State the preparation type.
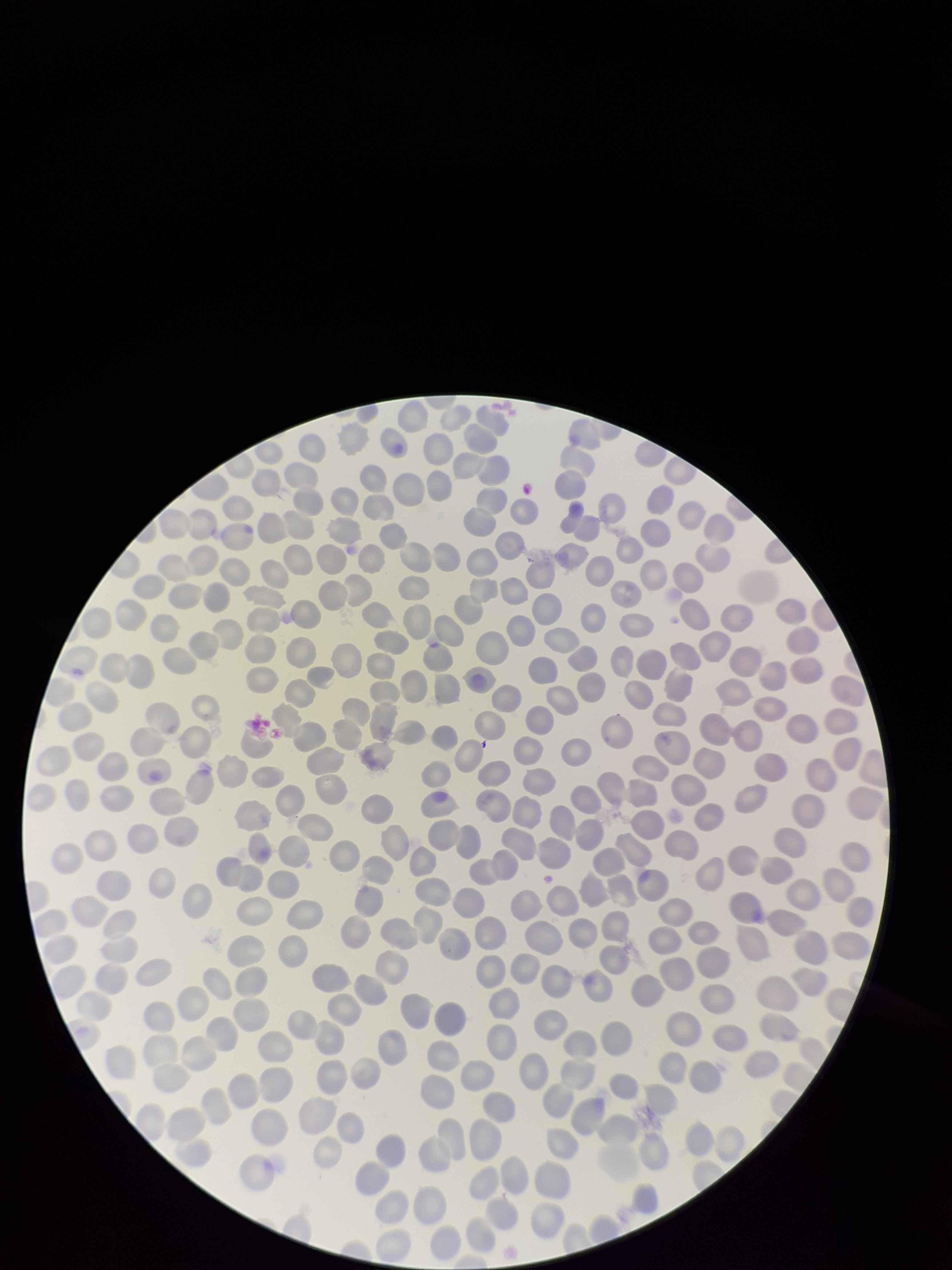
Thin.

Summary:
  - Patient malaria status: negative
  - Capture: smartphone photograph through the microscope eyepiece
  - Field of view: one from this slide
  - Image size: 952×1270 pixels
  - Parasitized red blood cells: none identified
  - Parasitized red blood cell count: 0
  - Stain: Giemsa
  - Red blood cell count: 302